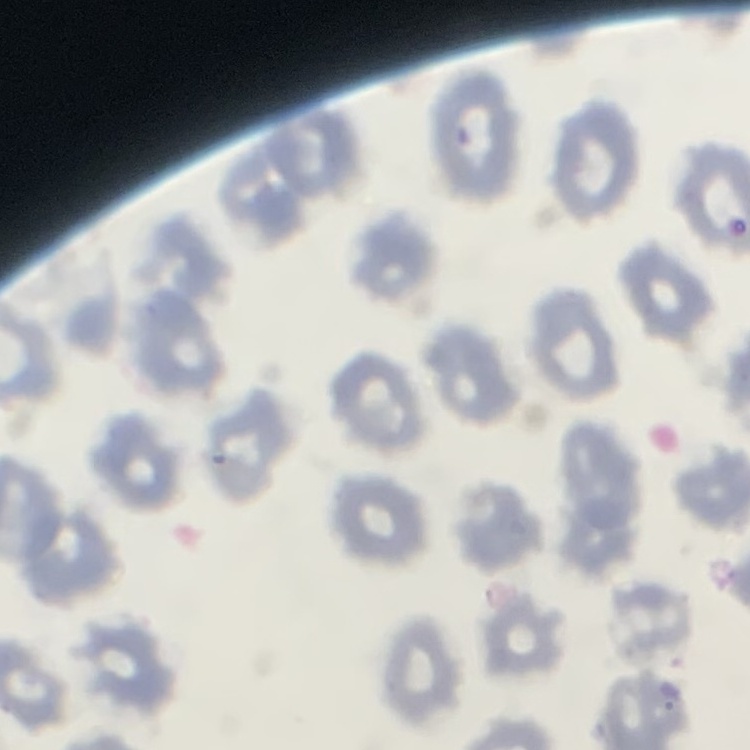

Summary:
  - Red blood cell morphology: no rouleaux formation
  - Preparation: thin blood film
  - Image type: square crop of a larger photomicrograph
  - Stain: Field's or Giemsa